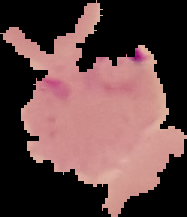
Summary:
  - Preparation: thin blood smear
  - Image size: 187×217 pixels
  - Image type: cell region segmented out of the field of view; surrounding area masked to black
  - Result: Plasmodium parasites identified